Locate every parasitized red blood cell.
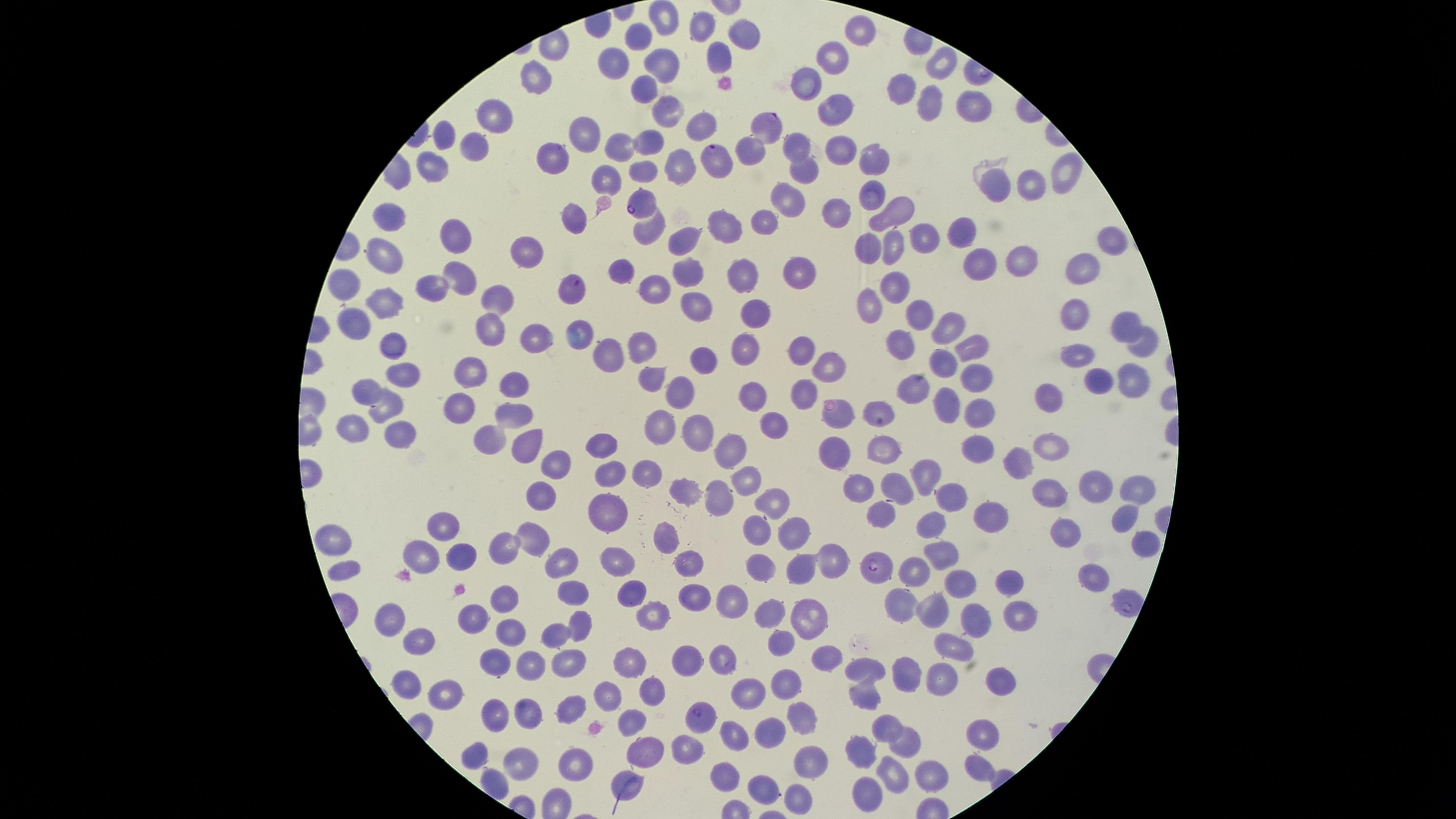
Approximate marker points as [x, y] in pixels.
Parasitized red blood cells: [767, 129], [717, 159], [642, 200], [574, 288], [878, 565], [701, 716].

visible region = circular
preparation = thin smear of blood
species = Plasmodium falciparum
field of view = single
image size = 1456×819 pixels
stain = Giemsa
capture = smartphone photograph through the microscope eyepiece
uninfected red blood cells = approximate marker points as [x, y] in pixels: [665, 15], [702, 21], [746, 29], [859, 30], [641, 37], [720, 52], [835, 55], [616, 59], [939, 64], [661, 65], [538, 77], [805, 83], [903, 84], [644, 87], [663, 102], [925, 103], [829, 104], [966, 106], [495, 112], [703, 124], [445, 130], [582, 131], [647, 136], [474, 139], [621, 143], [792, 145], [837, 148], [558, 156], [874, 158], [673, 159], [434, 163], [643, 168], [807, 169], [607, 177], [1066, 177], [997, 184], [1027, 186], [871, 190], [788, 198], [842, 210], [898, 210], [577, 213], [396, 218], [766, 218], [651, 225], [718, 225], [925, 234], [956, 234], [448, 235], [680, 241], [1111, 242], [867, 243], [891, 247], [529, 252], [387, 255], [1022, 257], [984, 260], [1083, 265], [686, 271], [798, 272], [743, 273], [625, 275], [454, 279], [351, 281], [651, 288], [894, 288], [430, 289], [870, 297], [491, 298], [384, 304], [694, 305], [761, 311], [916, 316], [359, 318], [1075, 322], [1122, 326], [492, 327], [942, 333], [537, 339], [641, 340], [901, 342], [395, 343], [1142, 343], [966, 346], [749, 347], [609, 352], [1079, 352], [804, 356], [701, 360], [938, 361], [829, 365], [405, 372], [468, 373], [1130, 375], [649, 376], [975, 376], [1091, 381], [516, 382], [909, 384], [803, 390], [371, 391], [680, 391], [1048, 393], [756, 394], [946, 404], [980, 404], [386, 409], [465, 410], [875, 410], [840, 418], [512, 419], [663, 422], [774, 424], [699, 427], [351, 430], [398, 434], [489, 437], [599, 442], [525, 444], [988, 447], [1052, 448], [732, 449], [883, 449], [833, 454], [1023, 459], [552, 462], [611, 468], [646, 470], [931, 475], [746, 479], [893, 482], [856, 484], [1098, 486], [1045, 490], [681, 491], [721, 492], [1133, 492], [954, 494], [535, 495], [767, 502], [606, 505], [990, 514], [877, 517], [1116, 518], [933, 522], [1059, 529], [442, 530], [754, 530], [533, 531], [797, 533], [664, 536], [335, 537], [503, 542], [940, 553], [459, 554], [420, 555], [559, 558], [686, 561], [757, 562], [796, 563], [346, 566], [615, 566], [830, 566], [916, 569], [1090, 573], [956, 580], [1007, 581], [635, 591], [692, 593], [573, 594], [735, 595], [506, 598], [940, 602], [902, 605], [771, 609], [1025, 611], [649, 615], [806, 616], [478, 617], [981, 617], [396, 620], [580, 625], [510, 631], [554, 632], [418, 638], [779, 640], [948, 642], [685, 656], [567, 660], [498, 661], [534, 661], [723, 661], [828, 662], [872, 662], [628, 665], [904, 672], [409, 678], [943, 678], [1001, 678], [780, 681], [446, 688], [654, 690], [752, 692], [865, 692], [605, 693], [573, 703], [499, 708], [533, 711], [630, 714], [798, 714], [774, 727], [891, 727], [985, 728], [736, 730], [908, 743], [866, 747], [640, 748], [474, 754], [684, 754], [810, 758], [573, 759], [516, 764], [976, 769], [725, 772], [894, 772], [931, 772], [762, 787], [865, 790], [798, 798]